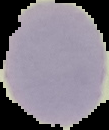
Result: no Plasmodium parasites seen. The area outside the segmented cell region is set to black. From a thin blood smear. Image is 109×130 pixels.